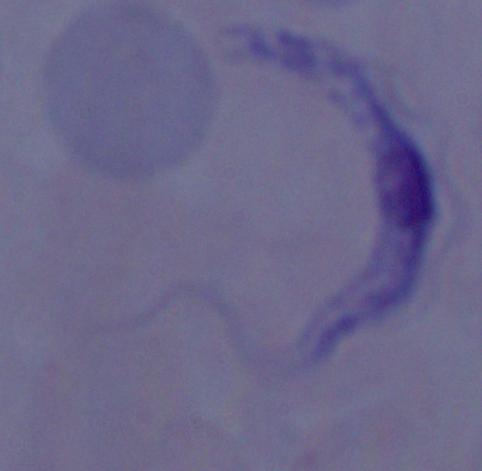

Summary:
  - Modality: micrograph
  - Magnification: 1000x
  - Identification: trypanosome